Identify the parasite.
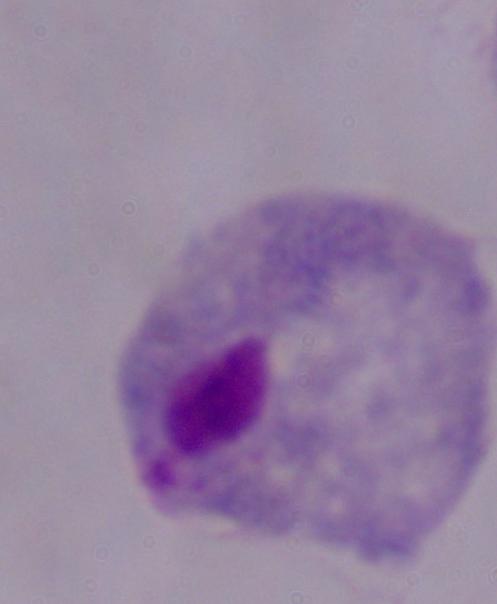
This is a trichomonad.

modality: photomicrograph
magnification: 1000x